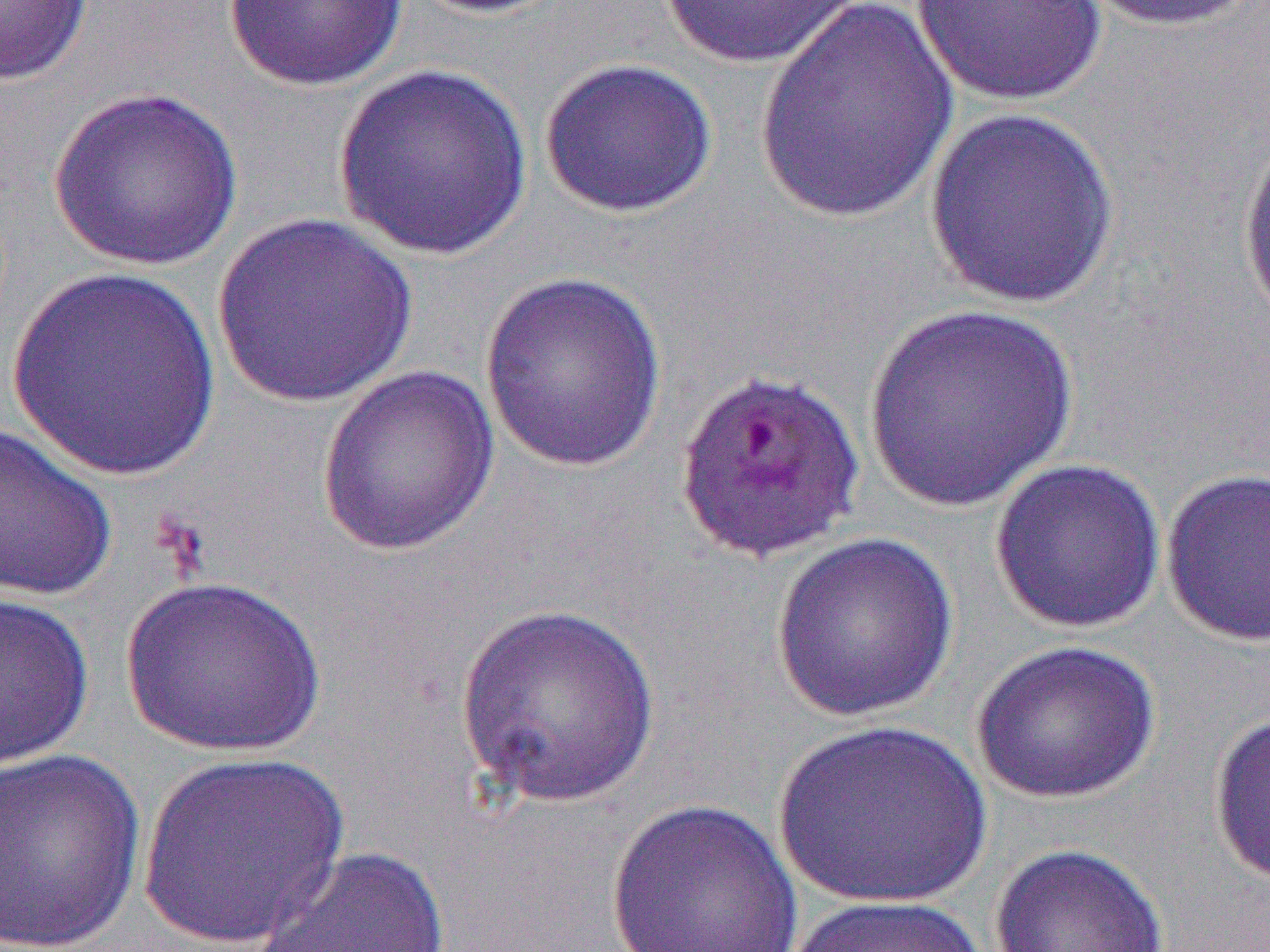
slide-level diagnosis = Plasmodium falciparum
uninfected red blood cell locations = approximate bounding boxes as named x1/y1/x2/y2 corners in pixels: (x1=0, y1=0, x2=95, y2=86), (x1=223, y1=0, x2=408, y2=93), (x1=403, y1=0, x2=569, y2=18), (x1=658, y1=0, x2=870, y2=69), (x1=910, y1=0, x2=1109, y2=108), (x1=1076, y1=0, x2=1261, y2=33), (x1=753, y1=1, x2=959, y2=225), (x1=539, y1=57, x2=718, y2=219), (x1=332, y1=63, x2=534, y2=261), (x1=47, y1=86, x2=244, y2=271), (x1=923, y1=106, x2=1122, y2=309), (x1=1236, y1=121, x2=1270, y2=340), (x1=210, y1=212, x2=418, y2=408), (x1=6, y1=269, x2=224, y2=483), (x1=478, y1=270, x2=669, y2=474), (x1=861, y1=305, x2=1080, y2=513), (x1=317, y1=364, x2=500, y2=556), (x1=0, y1=422, x2=118, y2=603), (x1=988, y1=457, x2=1167, y2=635), (x1=1160, y1=468, x2=1270, y2=647), (x1=770, y1=532, x2=959, y2=722), (x1=121, y1=575, x2=325, y2=757), (x1=0, y1=590, x2=95, y2=773), (x1=453, y1=603, x2=662, y2=810), (x1=971, y1=638, x2=1161, y2=805), (x1=1208, y1=710, x2=1270, y2=886), (x1=773, y1=720, x2=992, y2=910), (x1=0, y1=748, x2=146, y2=952), (x1=137, y1=750, x2=350, y2=949), (x1=606, y1=799, x2=803, y2=952), (x1=988, y1=843, x2=1170, y2=952), (x1=249, y1=845, x2=452, y2=952), (x1=781, y1=894, x2=989, y2=952)
image size = 1270×952 pixels
field of view = one of a larger specimen
preparation = thin blood film
magnification = 1000x
modality = optical microscopy